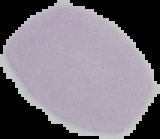
From a thin blood smear. Malaria status: uninfected. Image is 160×139 pixels. Segmented cell region on a black background.